Locate every Plasmodium falciparum-infected red blood cell.
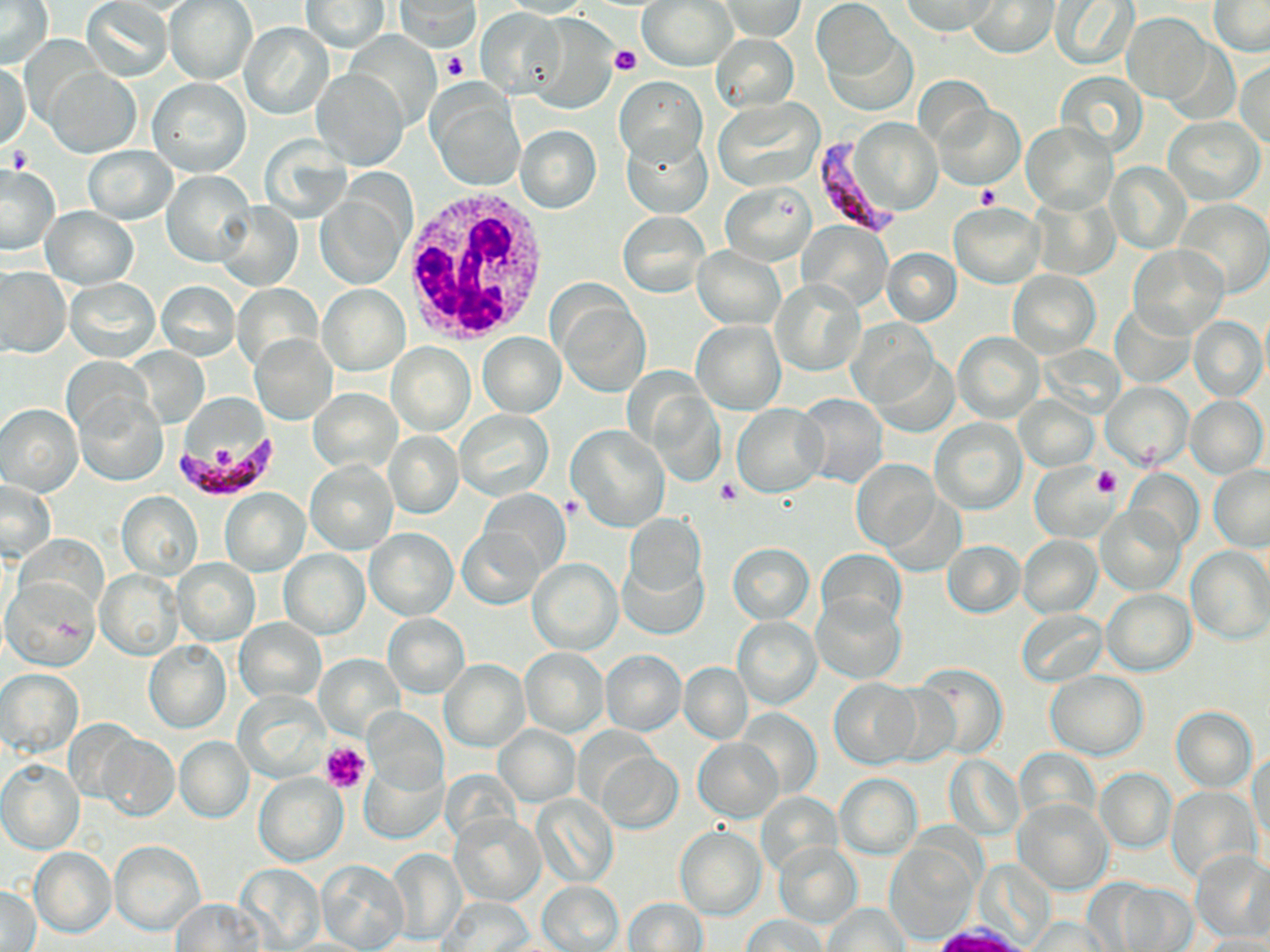

Approximate bounding boxes as [x1, y1, x2, y2] in pixels.
Plasmodium falciparum-infected red blood cells: [814, 134, 898, 232], [170, 430, 280, 499].

Uninfected red blood cell locations: [1, 0, 53, 68], [639, 0, 737, 70], [900, 0, 996, 37], [968, 0, 1060, 57], [1209, 0, 1269, 55], [82, 1, 173, 82], [165, 1, 257, 84], [302, 1, 389, 52], [396, 1, 480, 53], [717, 1, 806, 40], [812, 1, 900, 84], [1050, 1, 1139, 68], [479, 7, 566, 98], [1123, 12, 1212, 103], [240, 23, 334, 120], [824, 26, 916, 117], [345, 30, 441, 130], [711, 34, 799, 113], [1162, 39, 1237, 120], [1, 60, 31, 151], [1236, 60, 1270, 148], [312, 67, 406, 169], [45, 69, 140, 157], [1055, 70, 1148, 157], [614, 76, 707, 169], [147, 78, 250, 178], [426, 81, 526, 191], [714, 98, 824, 192], [933, 104, 1024, 188], [1163, 117, 1265, 205], [848, 118, 941, 215], [1023, 122, 1116, 214], [515, 125, 602, 214], [621, 129, 713, 218], [84, 146, 178, 224], [1106, 162, 1191, 254], [0, 164, 60, 255], [163, 170, 256, 267], [316, 180, 412, 289], [720, 182, 814, 266], [1029, 193, 1121, 280], [1172, 198, 1270, 298], [948, 202, 1044, 287], [216, 203, 301, 291], [41, 207, 138, 289], [618, 212, 708, 296], [798, 221, 892, 310], [692, 245, 785, 330], [1129, 245, 1228, 341], [882, 248, 961, 326], [0, 266, 69, 359], [1008, 271, 1099, 357], [65, 278, 159, 361], [770, 279, 865, 377], [157, 280, 240, 361], [231, 283, 324, 372], [318, 284, 410, 375], [552, 293, 651, 398], [1113, 304, 1194, 389], [1188, 316, 1266, 402], [847, 319, 938, 408], [692, 322, 785, 413], [954, 331, 1044, 423], [478, 332, 566, 418], [249, 334, 338, 424], [388, 342, 476, 436], [127, 348, 209, 426], [871, 351, 960, 436], [1102, 382, 1194, 471], [308, 389, 402, 472], [73, 390, 169, 487], [796, 393, 888, 489], [1017, 396, 1099, 470], [1185, 396, 1268, 480], [0, 403, 82, 496], [732, 403, 828, 497], [456, 409, 553, 500], [930, 418, 1026, 514], [568, 424, 669, 531], [385, 433, 463, 517], [305, 459, 399, 555], [851, 459, 939, 553], [1029, 464, 1116, 541], [1209, 465, 1270, 550], [1126, 470, 1203, 552], [1, 480, 56, 561], [877, 487, 969, 578], [477, 488, 569, 580], [221, 489, 309, 576], [117, 491, 204, 579], [1096, 504, 1187, 595], [623, 515, 707, 604], [365, 527, 458, 620], [457, 527, 547, 608], [1018, 534, 1102, 618], [940, 541, 1025, 618], [726, 542, 814, 623], [1186, 546, 1270, 645], [816, 549, 905, 629], [280, 550, 368, 638], [618, 552, 709, 642], [528, 557, 622, 655], [171, 558, 262, 646], [95, 569, 181, 660], [4, 577, 100, 671], [1102, 590, 1195, 674], [811, 594, 906, 684], [1017, 610, 1107, 686], [384, 613, 469, 697], [733, 617, 821, 709], [235, 619, 326, 703], [144, 640, 231, 733], [520, 647, 609, 736], [600, 649, 686, 735], [315, 656, 402, 738], [440, 659, 529, 751], [679, 662, 752, 743], [912, 662, 1008, 761], [1, 668, 84, 755], [1047, 670, 1147, 760], [829, 678, 923, 769], [878, 682, 959, 769], [235, 690, 330, 782], [736, 706, 820, 800], [1170, 706, 1257, 792], [361, 708, 447, 793], [495, 725, 579, 805], [95, 730, 178, 821], [175, 737, 254, 823], [693, 739, 784, 822], [1250, 748, 1269, 850], [1014, 749, 1098, 826], [595, 751, 682, 833], [944, 754, 1024, 839], [0, 760, 85, 854], [359, 761, 446, 843], [1094, 768, 1177, 853], [255, 773, 349, 867], [835, 773, 920, 857], [1165, 785, 1261, 882], [756, 792, 843, 875], [534, 794, 617, 889], [1015, 797, 1113, 893], [451, 815, 545, 905], [423, 825, 534, 947], [675, 826, 766, 919], [109, 840, 205, 933], [774, 841, 863, 929], [886, 842, 978, 943], [30, 847, 116, 938], [387, 847, 465, 946], [1189, 849, 1270, 942], [318, 860, 408, 951], [235, 865, 323, 949], [1102, 881, 1198, 952], [538, 882, 622, 951], [1, 884, 41, 951], [439, 897, 533, 950], [623, 898, 708, 951], [172, 899, 265, 950], [822, 903, 909, 951], [740, 915, 828, 952], [1026, 916, 1112, 951], [1201, 933, 1268, 952]. White blood cell locations: [398, 184, 557, 348]. Platelet locations: [610, 44, 640, 74], [442, 51, 469, 82], [5, 147, 33, 173], [975, 185, 1000, 207], [1092, 466, 1121, 497], [715, 477, 739, 505], [322, 743, 370, 792]. Slide-level diagnosis: Plasmodium falciparum. May-Grünwald-Giemsa stain. One field of a larger specimen. Thin blood film. Image is 1270×952 pixels. Optical microscopy. Captured at 1000x magnification.